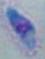
1000x magnification. Micrograph. Toxoplasma gondii is shown.